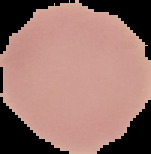
image type = cell region segmented out of the field of view; surrounding area masked to black
preparation = thin blood film
image size = 151×154 pixels
malaria status = uninfected